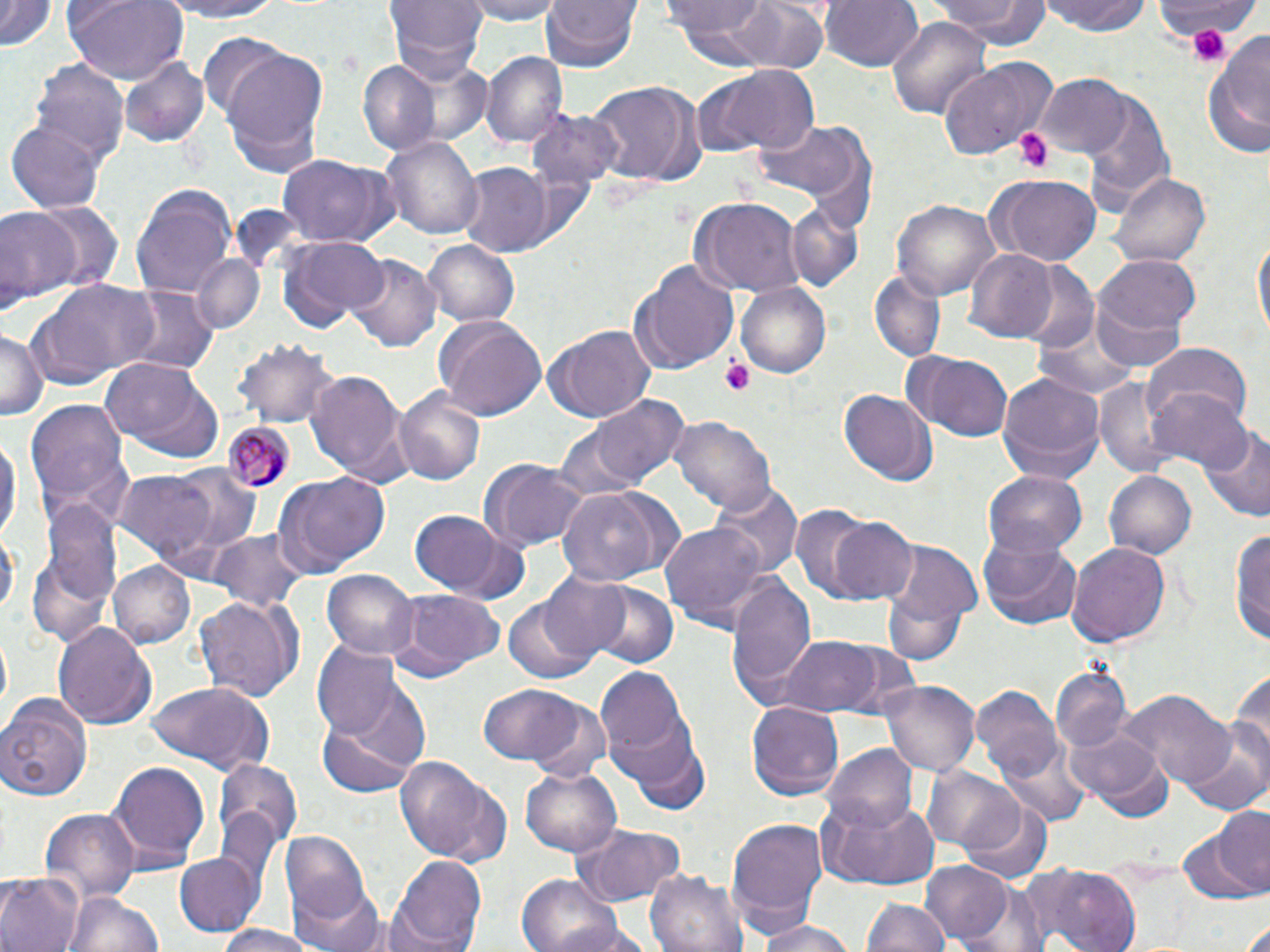 Approximate bounding boxes as (x1, y1, x2, y2) in pixels. Uninfected red blood cell locations: (1, 0, 56, 53), (62, 0, 189, 84), (150, 0, 288, 23), (387, 0, 487, 82), (461, 0, 570, 23), (540, 0, 641, 73), (667, 0, 779, 51), (737, 0, 830, 75), (819, 0, 923, 73), (931, 0, 1048, 48), (1043, 0, 1152, 37), (886, 16, 993, 117), (1204, 27, 1270, 163), (197, 35, 293, 116), (219, 49, 330, 174), (483, 52, 566, 148), (120, 56, 210, 145), (937, 59, 1056, 159), (31, 60, 128, 166), (359, 62, 439, 153), (697, 64, 823, 159), (1037, 74, 1134, 159), (582, 80, 699, 189), (1083, 92, 1175, 209), (527, 109, 624, 190), (747, 119, 872, 210), (8, 121, 104, 214), (384, 136, 483, 242), (276, 155, 395, 251), (457, 165, 554, 255), (1109, 168, 1211, 267), (984, 173, 1102, 267), (130, 184, 239, 299), (689, 198, 805, 295), (891, 198, 1000, 303), (29, 199, 122, 295), (785, 202, 865, 293), (0, 208, 79, 307), (278, 235, 388, 331), (1252, 235, 1269, 346), (421, 239, 520, 326), (963, 249, 1059, 342), (190, 254, 267, 336), (347, 255, 441, 351), (1095, 255, 1201, 339), (628, 261, 738, 375), (1013, 264, 1099, 356), (869, 268, 947, 363), (30, 279, 163, 383), (736, 281, 833, 380), (124, 286, 216, 377), (433, 315, 548, 422), (1034, 318, 1143, 400), (0, 326, 43, 422), (544, 326, 653, 424), (233, 337, 343, 428), (1143, 341, 1252, 428), (901, 352, 1014, 442), (99, 357, 221, 463), (307, 367, 407, 483), (997, 370, 1105, 486), (1093, 378, 1185, 475), (394, 386, 483, 486), (838, 388, 936, 486), (1147, 388, 1253, 479), (588, 393, 688, 490), (23, 402, 134, 527), (670, 417, 776, 517), (552, 421, 653, 505), (1200, 427, 1270, 525), (0, 428, 19, 548), (479, 459, 589, 552), (164, 464, 263, 558), (117, 470, 222, 561), (1104, 470, 1196, 561), (984, 471, 1086, 556), (273, 473, 390, 577), (710, 481, 801, 580), (553, 485, 684, 585), (38, 497, 121, 626), (789, 504, 877, 603), (407, 511, 523, 600), (828, 516, 918, 605), (659, 521, 775, 630), (1232, 522, 1270, 649), (0, 526, 16, 626), (206, 528, 310, 613), (978, 536, 1082, 630), (881, 540, 983, 647), (1067, 541, 1173, 648), (107, 560, 194, 647), (324, 570, 419, 662), (727, 572, 817, 701), (537, 573, 630, 662), (586, 581, 680, 669), (396, 590, 504, 673), (195, 596, 297, 703), (504, 600, 598, 683), (55, 622, 154, 731), (774, 632, 891, 718), (311, 644, 406, 740), (1229, 661, 1270, 775), (595, 663, 692, 766), (1050, 668, 1130, 754), (881, 679, 979, 779), (146, 683, 274, 772), (477, 683, 587, 766), (972, 686, 1068, 791), (1124, 690, 1236, 791), (0, 693, 93, 803), (526, 699, 613, 785), (747, 701, 843, 803), (319, 704, 424, 797), (615, 723, 711, 810), (1186, 724, 1270, 817), (1067, 729, 1171, 817), (823, 744, 917, 833), (393, 755, 514, 868), (108, 760, 212, 870), (215, 761, 304, 850), (924, 767, 1023, 852), (519, 770, 621, 857), (819, 796, 942, 890), (963, 799, 1055, 886), (40, 808, 139, 897), (1188, 812, 1270, 902), (725, 817, 827, 937), (569, 822, 688, 909), (281, 834, 371, 930), (173, 851, 263, 936), (390, 853, 486, 951), (918, 860, 1012, 944), (1013, 865, 1142, 952), (646, 866, 747, 952), (0, 875, 82, 952), (517, 875, 629, 952), (294, 882, 386, 952), (64, 889, 164, 952), (863, 899, 951, 952), (750, 916, 856, 952), (209, 924, 320, 952). Plasmodium malariae-infected red blood cell locations: (223, 420, 293, 491). Platelet locations: (1165, 3, 1245, 64), (1187, 23, 1233, 67), (1015, 127, 1053, 172), (721, 357, 754, 396). Slide-level diagnosis: Plasmodium malariae. Light microscopy. 1000x magnification. Single field of view. Image is 1270×952 pixels. Thin blood film. May-Grünwald-Giemsa stain.